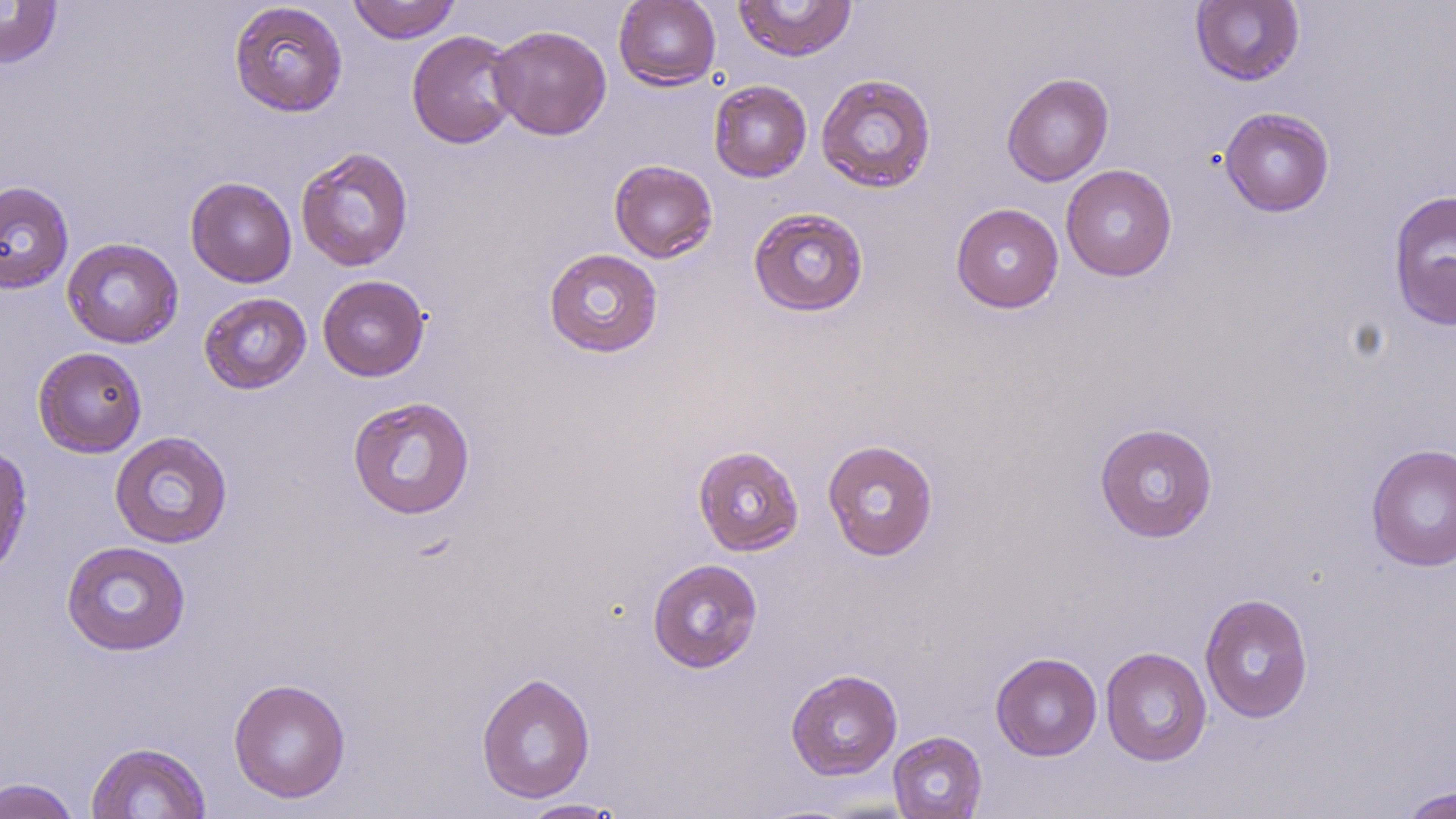
Summary:
  - Coordinate format: approximate bounding boxes as [x1, y1, x2, y2] in pixels
  - Uninfected red blood cell locations: [347, 0, 461, 44], [613, 0, 721, 90], [734, 0, 857, 62], [1190, 0, 1305, 86], [0, 1, 63, 69], [229, 2, 348, 117], [489, 24, 612, 140], [406, 30, 521, 149], [1002, 72, 1114, 186], [816, 73, 937, 193], [709, 80, 812, 183], [1220, 107, 1335, 217], [295, 146, 415, 272], [608, 159, 718, 263], [1060, 164, 1177, 282], [185, 176, 297, 288], [0, 180, 74, 294], [1387, 188, 1456, 332], [951, 203, 1064, 314], [748, 207, 869, 317], [61, 238, 184, 348], [543, 247, 663, 358], [317, 275, 430, 381], [198, 292, 312, 394], [32, 346, 148, 458], [347, 396, 476, 519], [1094, 422, 1219, 543], [108, 430, 233, 549], [822, 439, 939, 561], [1366, 442, 1456, 572], [0, 443, 34, 581], [692, 444, 804, 556], [61, 540, 192, 656], [647, 558, 763, 673], [1199, 593, 1314, 724], [1100, 646, 1212, 767], [990, 652, 1102, 761], [785, 668, 903, 781], [476, 671, 596, 804], [228, 677, 351, 804], [887, 730, 987, 819], [85, 741, 212, 819], [0, 776, 83, 819], [1397, 785, 1456, 819], [520, 799, 624, 818]
  - Slide-level diagnosis: no evidence of blood parasites
  - Field of view: single
  - Preparation: thin blood smear
  - Stain: May-Grünwald-Giemsa
  - Image size: 1456×819 pixels
  - Modality: optical microscopy
  - Magnification: 1000x